Identify the blood parasite species.
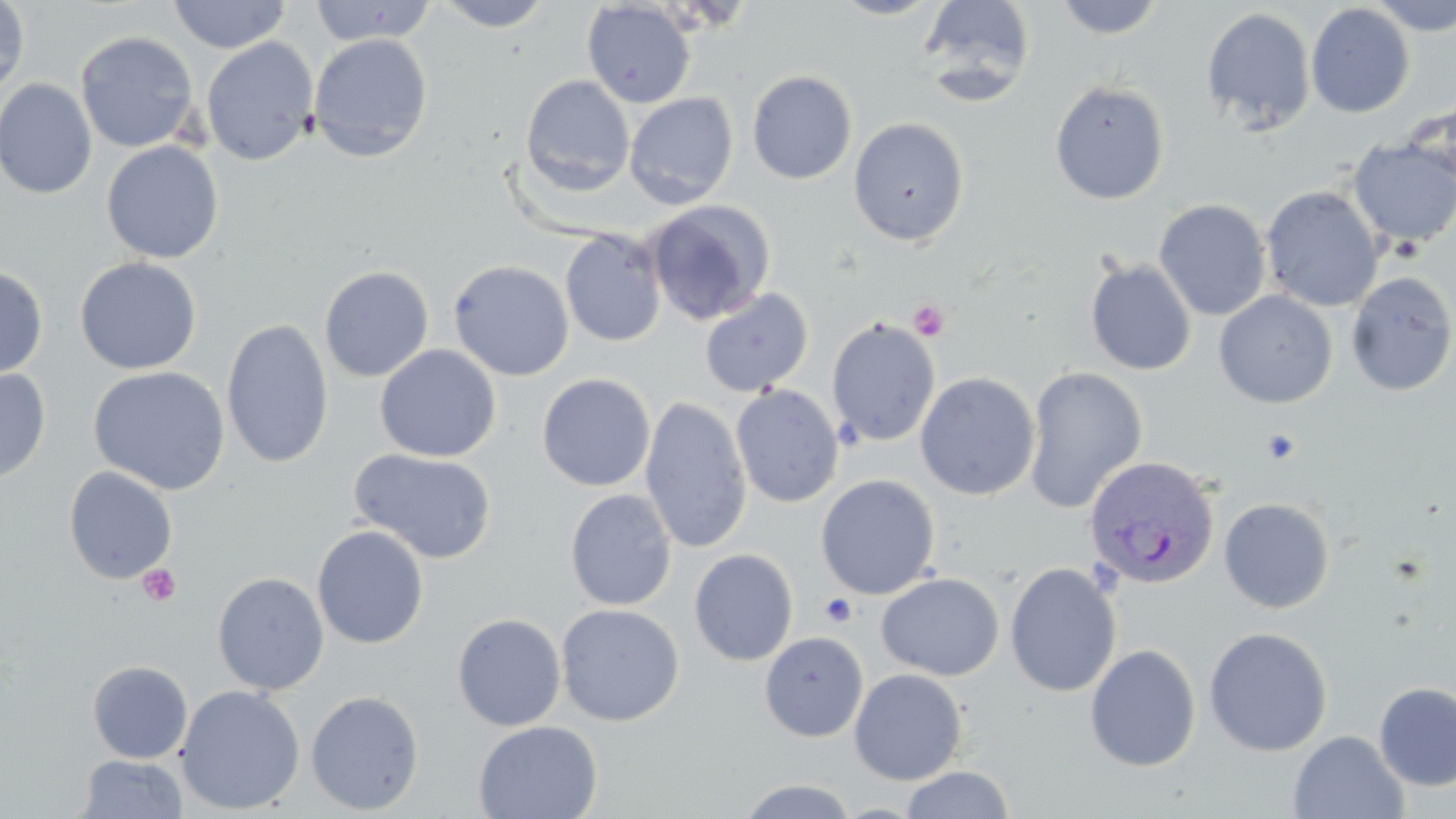
Plasmodium vivax.

modality = light microscopy
Plasmodium vivax-infected red blood cell locations = approximate bounding boxes as (x1, y1, x2, y2) in pixels: (1084, 455, 1220, 590)
field of view = one of a larger specimen
stain = May-Grünwald-Giemsa
magnification = 1000x
platelet locations = approximate bounding boxes as (x1, y1, x2, y2) in pixels: (908, 299, 950, 341), (1260, 427, 1301, 465), (138, 564, 181, 607), (819, 593, 858, 626)
uninfected red blood cell locations = approximate bounding boxes as (x1, y1, x2, y2) in pixels: (167, 0, 291, 54), (310, 0, 437, 46), (433, 0, 555, 32), (828, 0, 947, 20), (917, 0, 1037, 106), (1051, 0, 1168, 39), (1365, 0, 1456, 36), (0, 1, 30, 97), (582, 1, 696, 109), (1305, 3, 1416, 118), (1201, 7, 1316, 134), (75, 30, 199, 153), (308, 34, 433, 163), (201, 36, 320, 167), (746, 69, 858, 185), (520, 75, 634, 195), (0, 78, 97, 199), (1049, 80, 1170, 205), (624, 92, 738, 209), (1406, 95, 1456, 198), (848, 117, 969, 246), (1347, 138, 1456, 250), (101, 141, 224, 264), (1260, 185, 1384, 312), (1154, 199, 1272, 321), (644, 200, 776, 325), (560, 229, 667, 347), (75, 257, 202, 375), (1084, 257, 1197, 376), (448, 259, 574, 381), (0, 265, 49, 380), (319, 266, 434, 382), (1346, 272, 1456, 396), (699, 288, 814, 398), (1213, 290, 1338, 409), (221, 318, 334, 469), (826, 318, 941, 447), (374, 344, 501, 462), (89, 366, 230, 496), (1023, 366, 1148, 513), (0, 367, 52, 484), (915, 372, 1040, 500), (537, 373, 656, 492), (731, 384, 844, 508), (640, 396, 752, 554), (350, 448, 497, 563), (63, 466, 178, 585), (815, 474, 940, 600), (565, 488, 678, 611), (1219, 497, 1336, 613), (312, 525, 430, 649), (689, 548, 799, 666), (1004, 561, 1122, 698), (212, 572, 329, 695), (876, 572, 1004, 680), (556, 604, 684, 725), (452, 613, 566, 732), (1203, 626, 1333, 757), (759, 631, 868, 743), (1084, 643, 1201, 772), (87, 660, 193, 764), (849, 667, 968, 785), (1373, 681, 1456, 791), (175, 684, 305, 815), (305, 690, 425, 815), (474, 720, 602, 819), (1288, 730, 1408, 819), (78, 754, 188, 817), (899, 766, 1016, 819), (735, 778, 861, 819)
image size = 1456×819 pixels
preparation = thin blood film